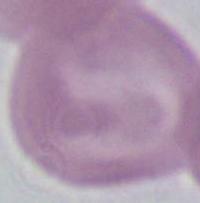

1000x magnification. A red blood cell is shown. Micrograph.